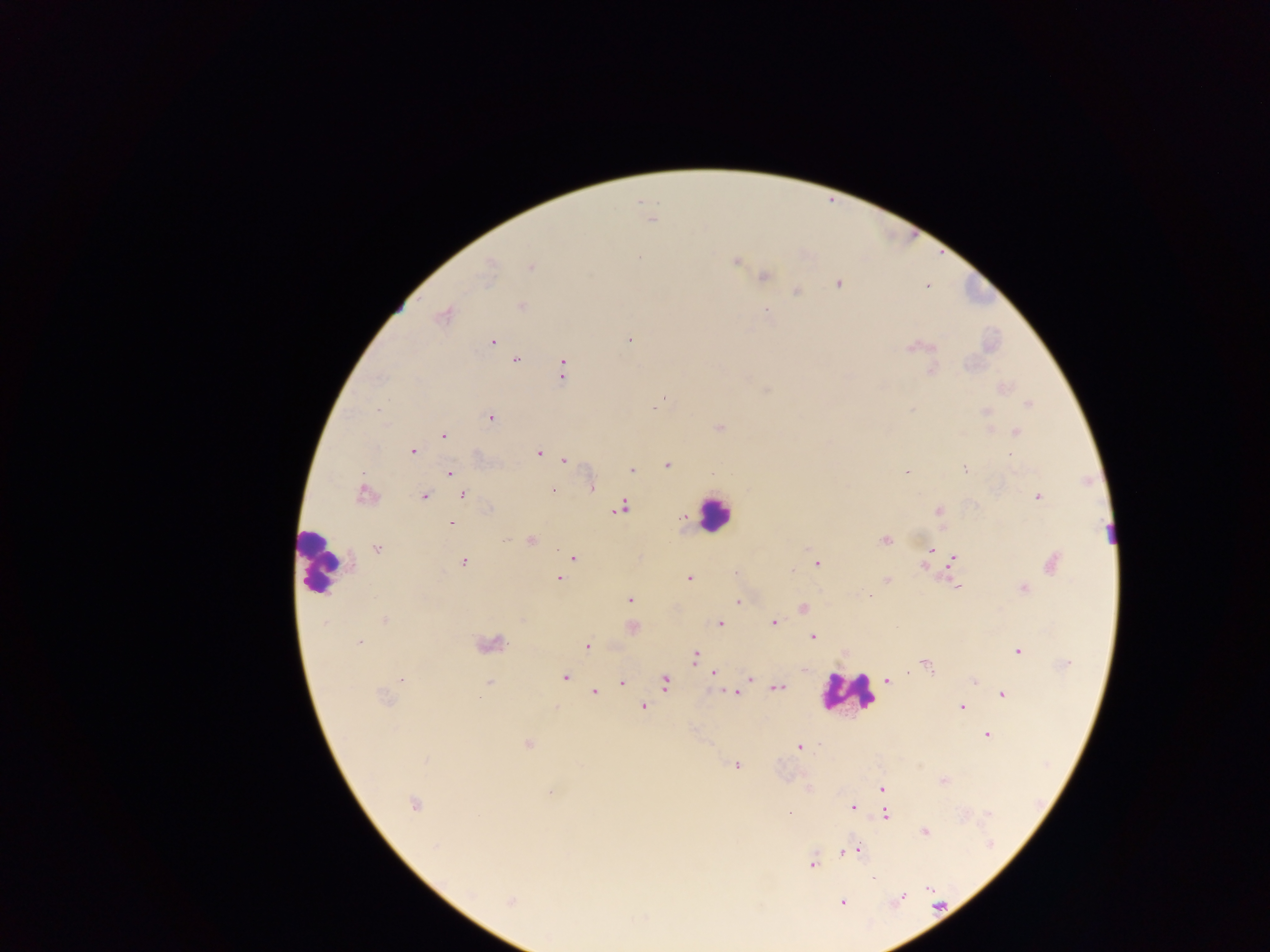
Approximate centers as (x, y) in pixels.
Summary:
  - Plasmodium parasite locations: (651, 218), (638, 257), (735, 261), (489, 267), (531, 267), (762, 276), (838, 284), (926, 286), (796, 291), (520, 305), (767, 310), (442, 315), (629, 339), (492, 342), (913, 347), (515, 359), (563, 369), (932, 370), (1002, 387), (1028, 404), (655, 406), (986, 411), (490, 417), (719, 428), (1016, 431), (443, 435), (413, 451), (538, 453), (1011, 455), (564, 460), (668, 464), (965, 468), (630, 470), (906, 471), (450, 472), (591, 485), (552, 490), (365, 494), (423, 495), (463, 495), (1037, 496), (621, 507), (939, 510), (681, 517), (451, 523), (885, 540), (530, 541), (376, 548), (931, 550), (573, 557), (952, 559), (463, 561), (817, 562), (1051, 562), (924, 566), (689, 578), (558, 579), (886, 580), (958, 587), (1023, 589), (869, 596), (629, 599), (738, 601), (803, 608), (385, 620), (773, 622), (719, 623), (631, 627), (814, 637), (359, 642), (488, 643), (587, 646), (845, 650), (1018, 651), (694, 655), (925, 663), (804, 671), (713, 672), (565, 677), (749, 677), (401, 679), (887, 679), (973, 679), (664, 682), (488, 683), (621, 683), (776, 688), (593, 692), (734, 692), (1002, 694), (383, 699), (644, 705), (960, 707), (555, 709), (987, 733), (528, 743), (798, 746), (736, 765), (943, 780), (882, 788), (550, 791), (413, 803), (852, 807), (788, 814), (886, 814), (924, 830), (859, 849), (844, 851), (812, 863), (509, 901), (842, 901)
  - Leukocyte locations: (714, 513), (316, 562), (846, 693)
  - Field of view: single
  - Preparation: thick blood film
  - Country: Ghana
  - Capture: mobile-phone photograph through a microscope
  - Image size: 1270×952 pixels